Identify the parasite.
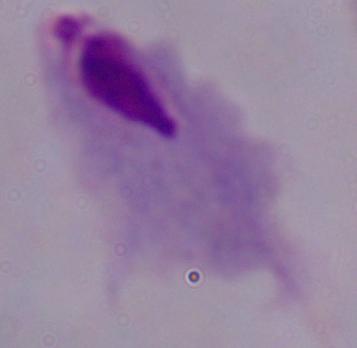
This is a trichomonad.

magnification = 1000x
modality = micrograph